Name the parasite shown.
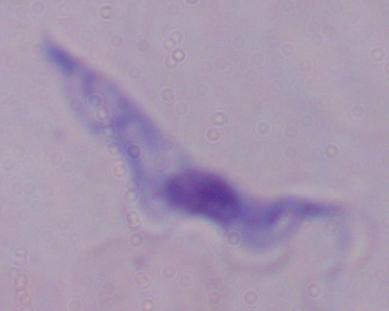

This is a trypanosome.

Summary:
  - Modality: photomicrograph
  - Magnification: 1000x